Point out each leukocyte.
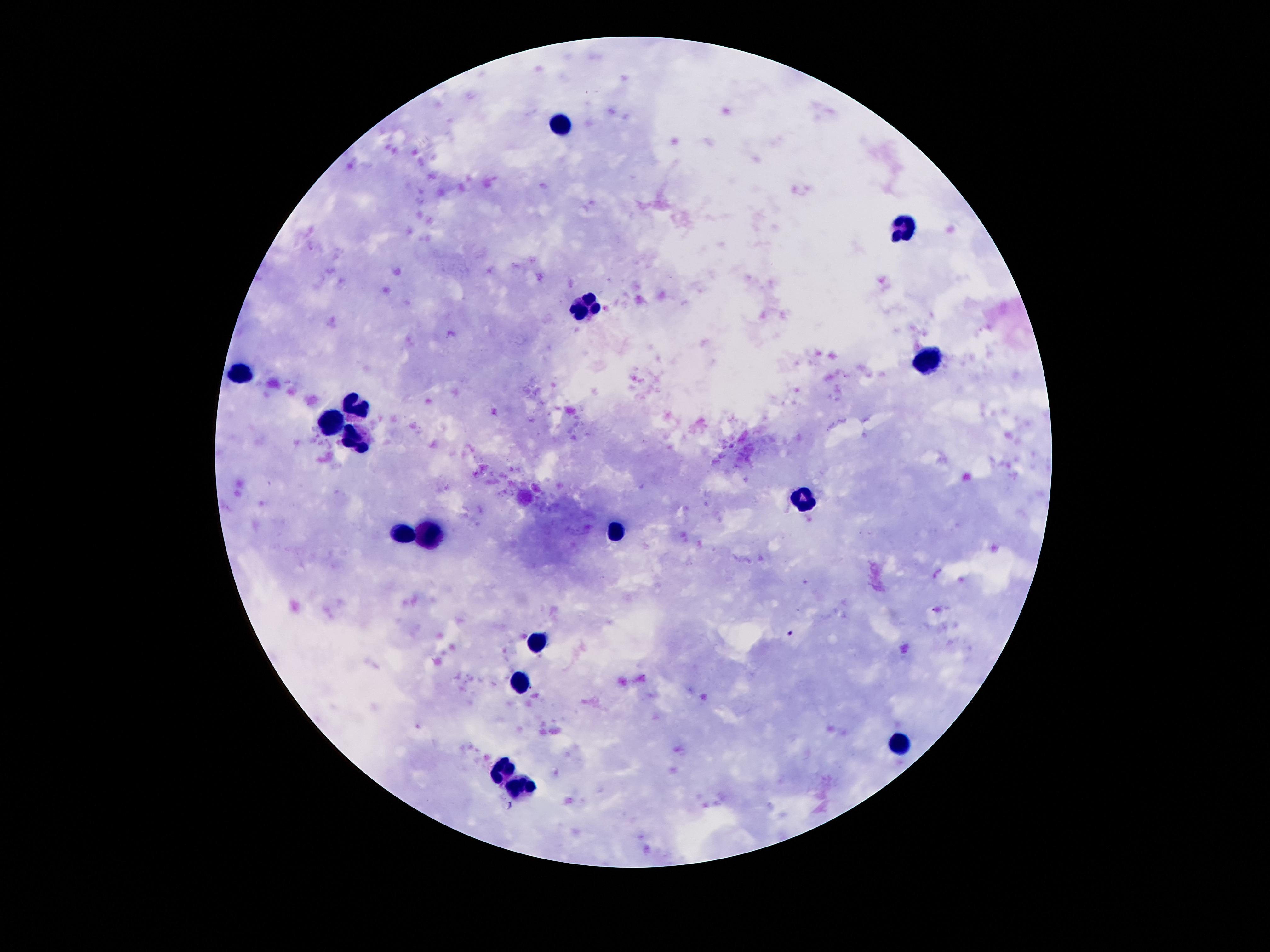
Approximate centers as {x, y} in pixels.
Leukocytes: {566, 121}, {908, 229}, {587, 309}, {928, 362}, {238, 375}, {355, 405}, {333, 425}, {357, 440}, {803, 496}, {617, 534}, {404, 536}, {428, 537}, {533, 644}, {518, 687}, {900, 748}, {503, 771}, {518, 786}.

Patient malaria status: negative. Single field of view. Photographed through the microscope eyepiece with a smartphone camera. Giemsa stain. 100x magnification. Thick blood smear. Image is 1270×952 pixels.